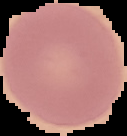 Image is 127×136 pixels. Result: negative for malaria parasites. Cell region segmented out of the field of view; the surrounding area is masked to black. From a thin blood film.